Comment on the morphology of the red blood cells.
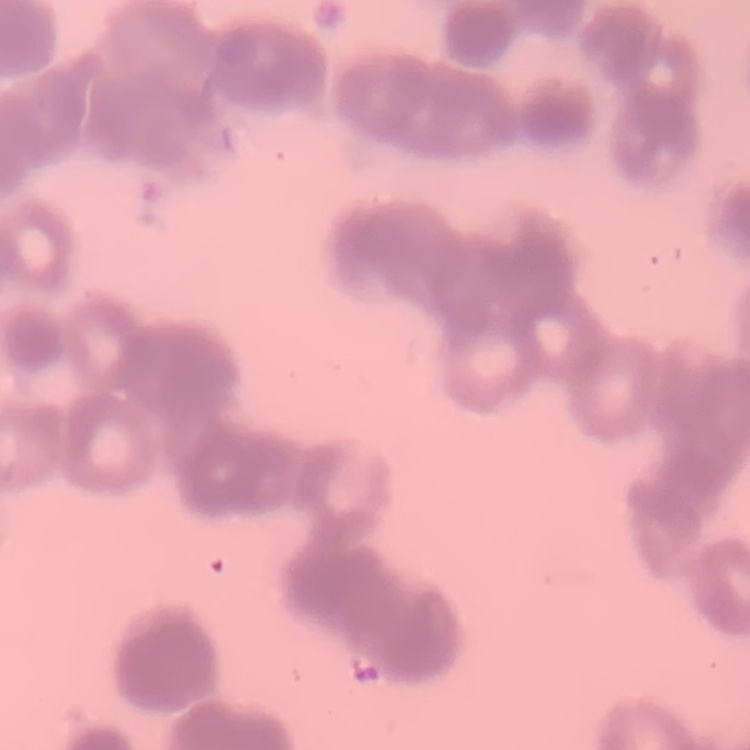

They show rouleaux formation.

Thin blood film. Stained with either Field's or Giemsa. One tile cut from a larger photomicrograph.